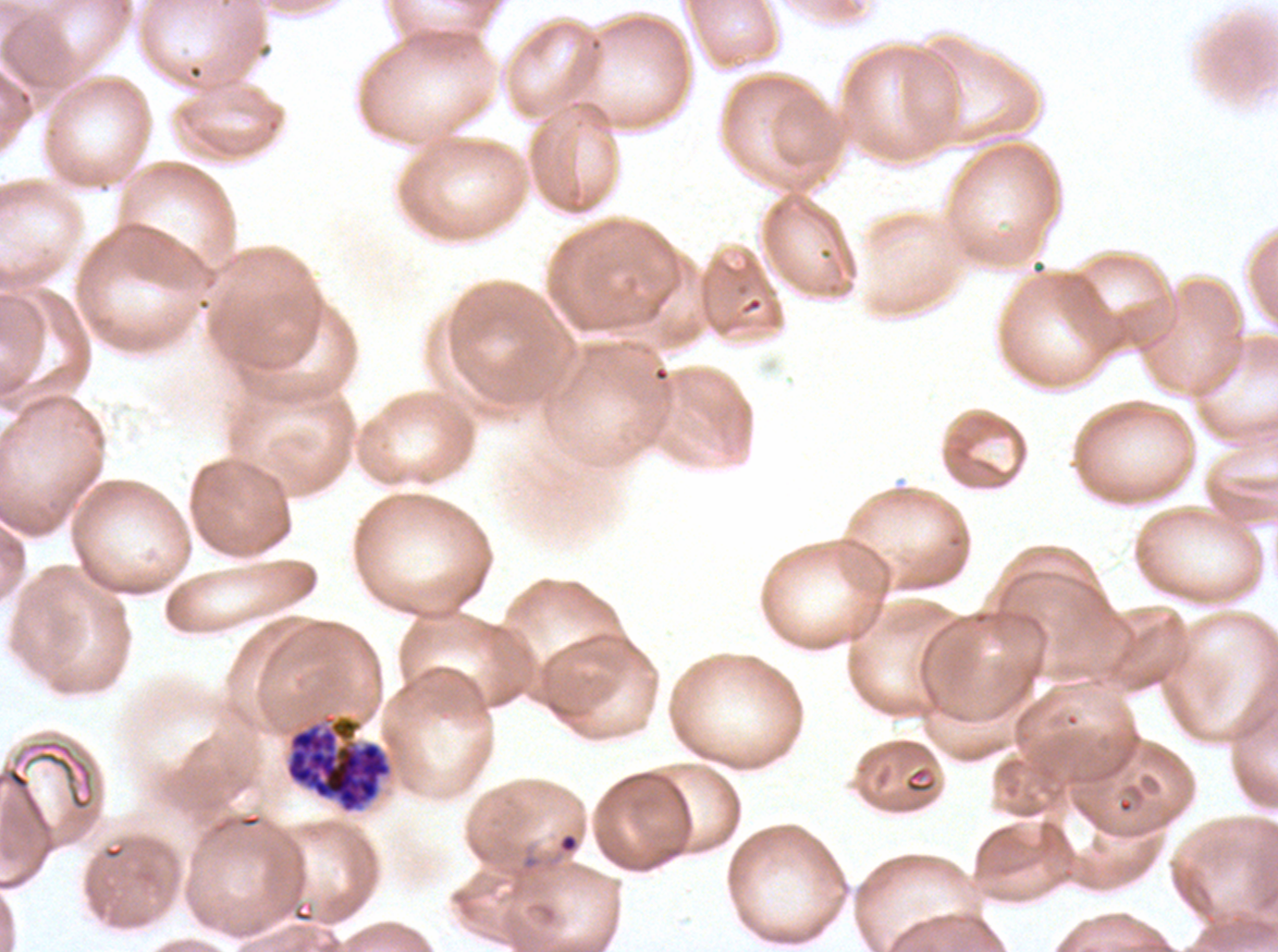

Approximate bounding boxes as {x1, y1, x2, y2} in pixels. Ring locations: {510, 830, 582, 882}. Segmenter locations: {284, 712, 394, 814}. Image is 1278×952 pixels. Thin blood film. Plasmodium falciparum cultured ex vivo for 24 to 48 hours, from a patient in The Gambia. Giemsa-stained preparation. Life-cycle stages observed: ring, segmenter. One sub-image of a larger composite.